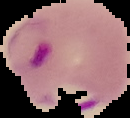
Summary:
  - Image size: 130×118 pixels
  - Preparation: thin blood film
  - Image type: segmented cell region with the area outside set to black
  - Result: Plasmodium parasites identified